Describe the morphology of the erythrocytes.
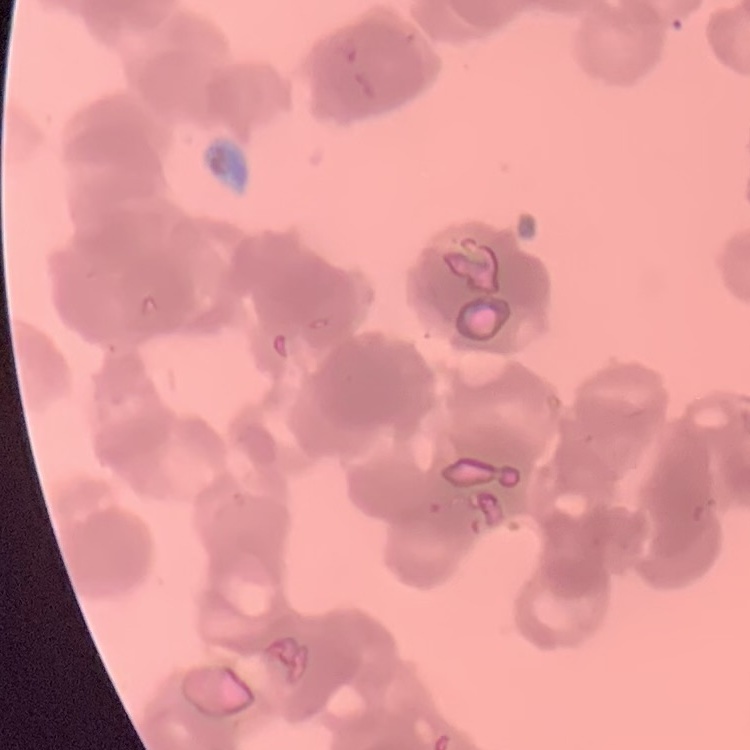

Rouleaux formation.

Stained with either Field's or Giemsa. Thin peripheral smear. Square crop of a larger photomicrograph.